Describe the morphology of the erythrocytes.
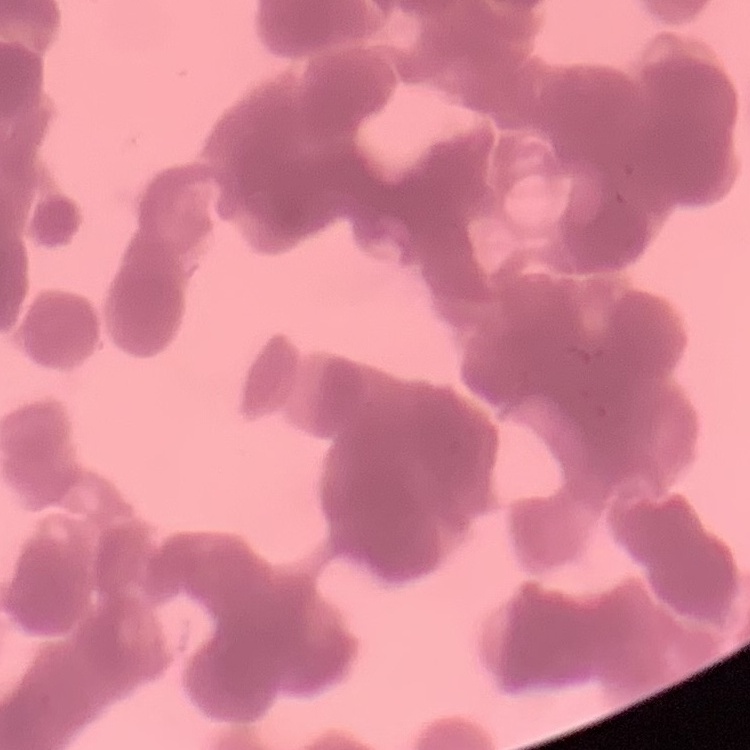

Rouleaux formation.

Summary:
  - Stain: Field's or Giemsa
  - Preparation: thin peripheral smear
  - Image type: one tile cut from a larger photomicrograph